Comment on the morphology of the erythrocytes.
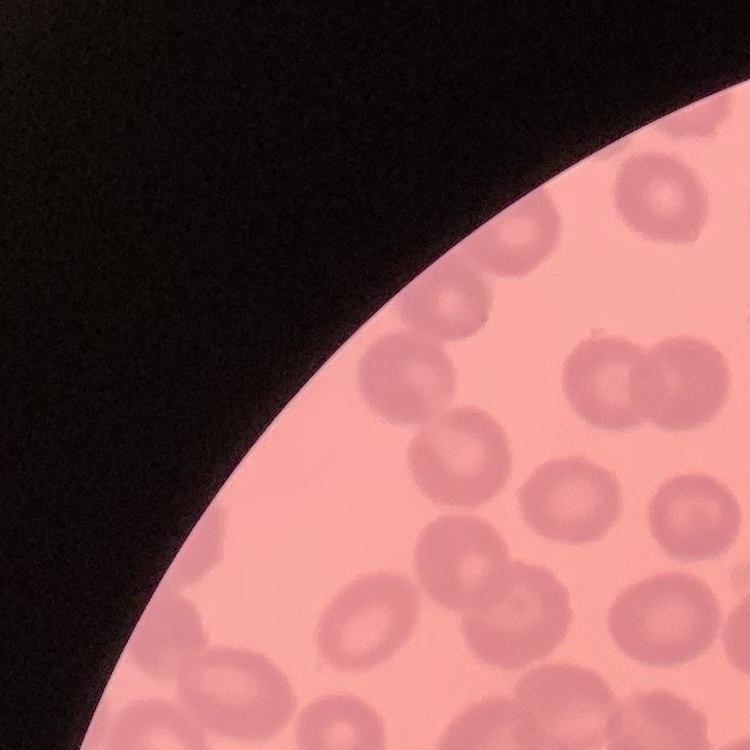
No rouleaux formation.

Square crop of a larger photomicrograph. Thin blood film. Stained with either Field's or Giemsa.